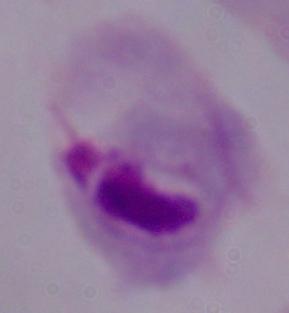

magnification = 1000x
modality = photomicrograph
identification = trichomonad